Assess the morphology of the erythrocytes.
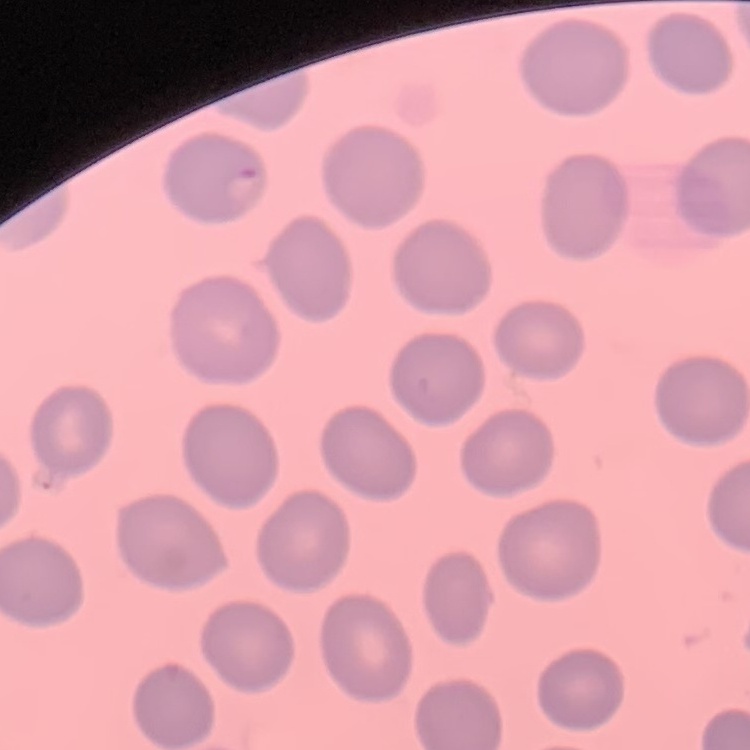
No rouleaux formation.

Summary:
  - Image type: square crop of a larger photomicrograph
  - Preparation: thin blood film
  - Stain: Field's or Giemsa